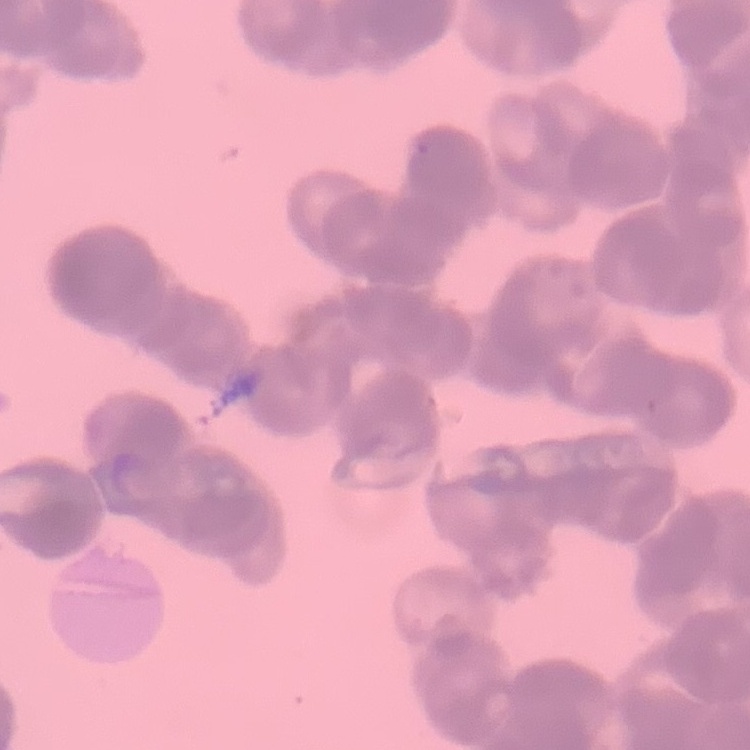

erythrocyte morphology = rouleaux formation
preparation = thin peripheral smear
stain = Field's or Giemsa
image type = one tile cut from a larger photomicrograph